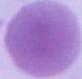

Photomicrograph. An erythrocyte is seen. 1000x magnification.